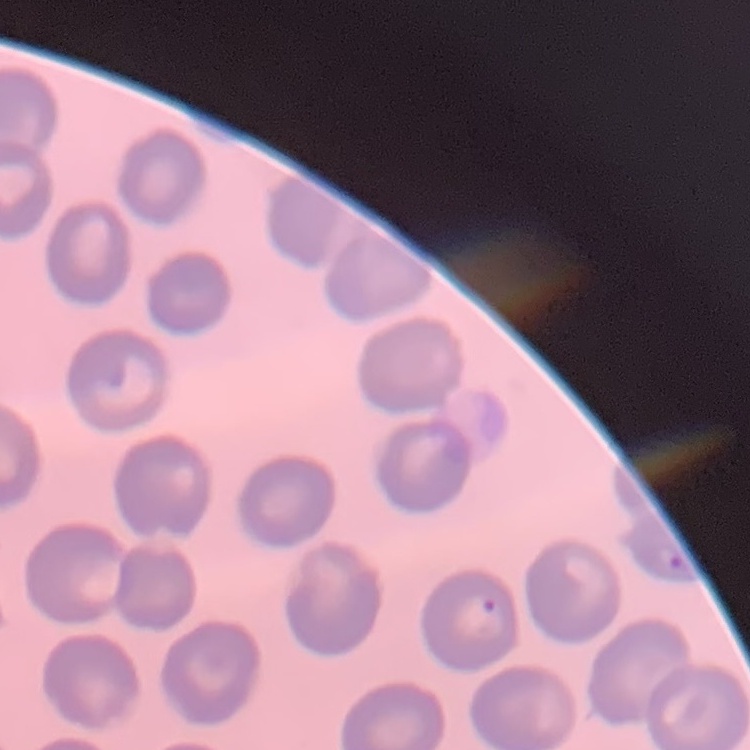

Summary:
  - Erythrocyte morphology: no rouleaux formation
  - Image type: square crop of a larger photomicrograph
  - Preparation: thin blood film
  - Stain: Field's or Giemsa